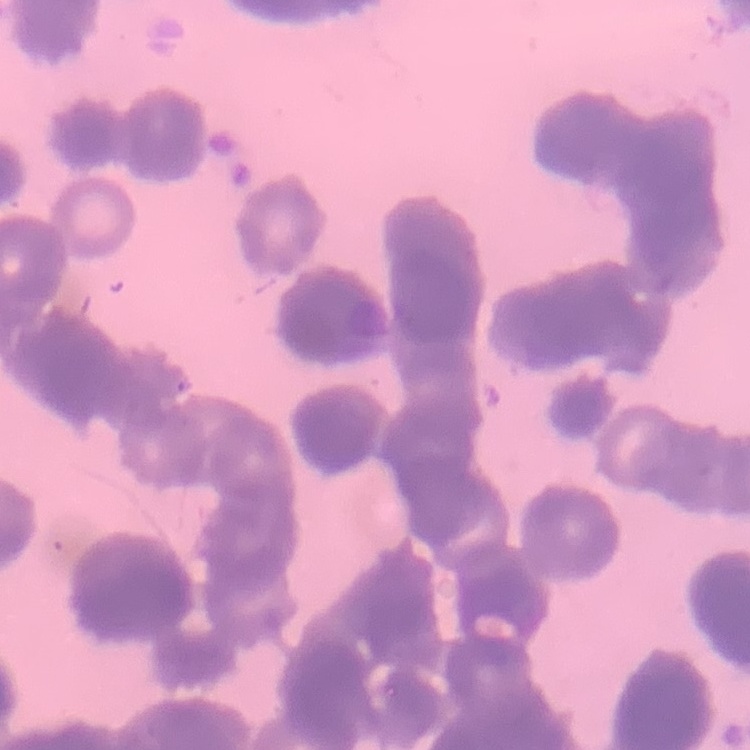

erythrocyte morphology = rouleaux formation
image type = one tile cut from a larger photomicrograph
preparation = thin peripheral smear
stain = Field's or Giemsa